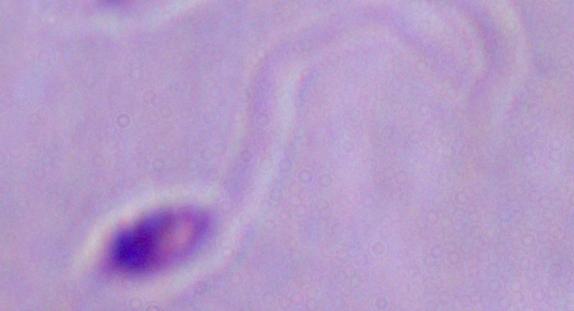

Summary:
  - Identification: Leishmania
  - Modality: photomicrograph
  - Magnification: 1000x